Comment on the morphology of the red blood cells.
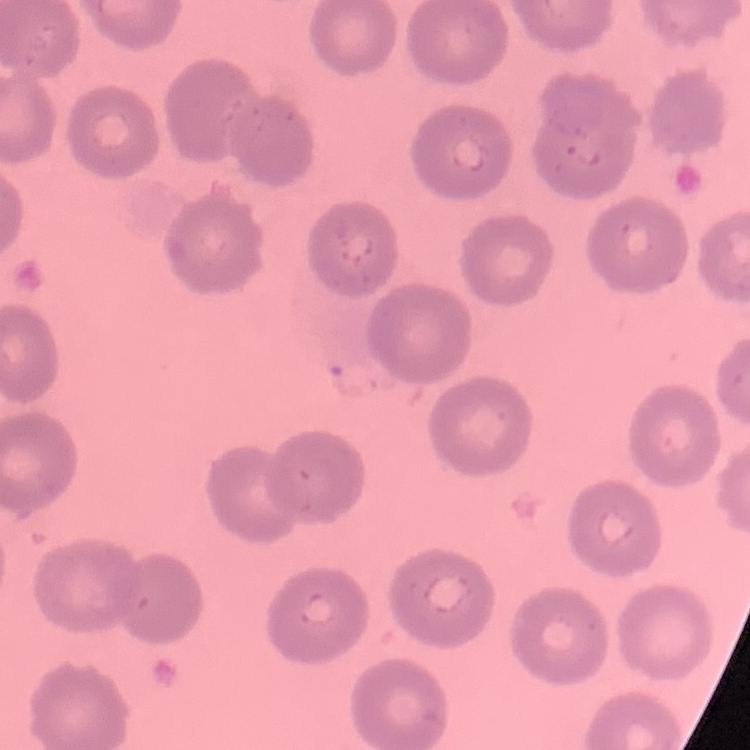
They show no rouleaux formation.

Summary:
  - Preparation: thin blood smear
  - Image type: one tile cut from a larger photomicrograph
  - Stain: Field's or Giemsa